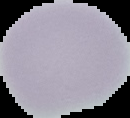
Result: no Plasmodium parasites seen. From a thin blood smear. Cell region segmented out of the field of view; the surrounding area is masked to black. Image is 130×118 pixels.